State which parasite is depicted.
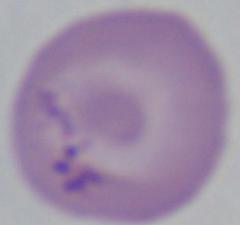

This is Babesia.

Photomicrograph. Captured at 1000x magnification.